Describe the morphology of the red blood cells.
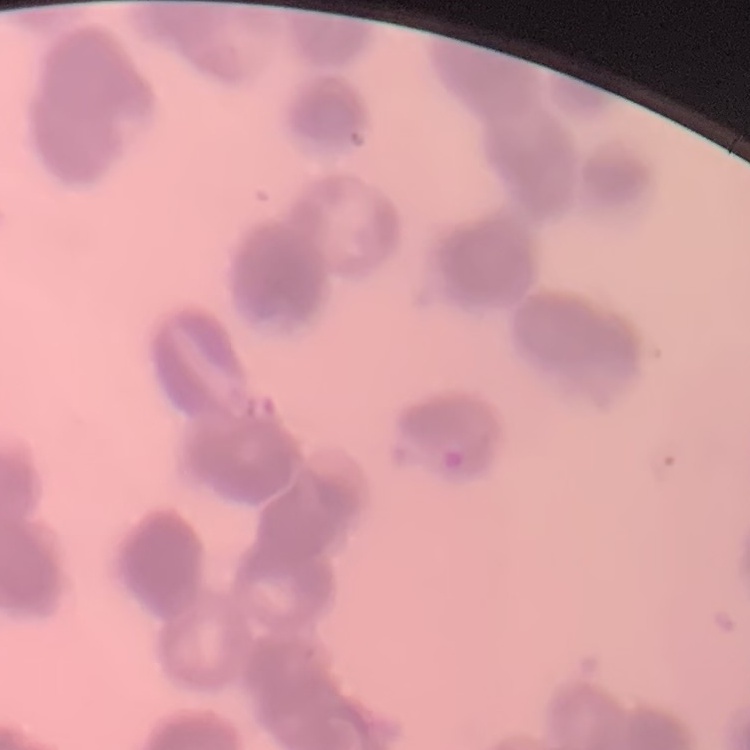

They show rouleaux formation.

Summary:
  - Stain: Field's or Giemsa
  - Image type: square crop of a larger photomicrograph
  - Preparation: thin blood smear